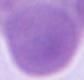
identification = erythrocyte
modality = photomicrograph
magnification = 1000x